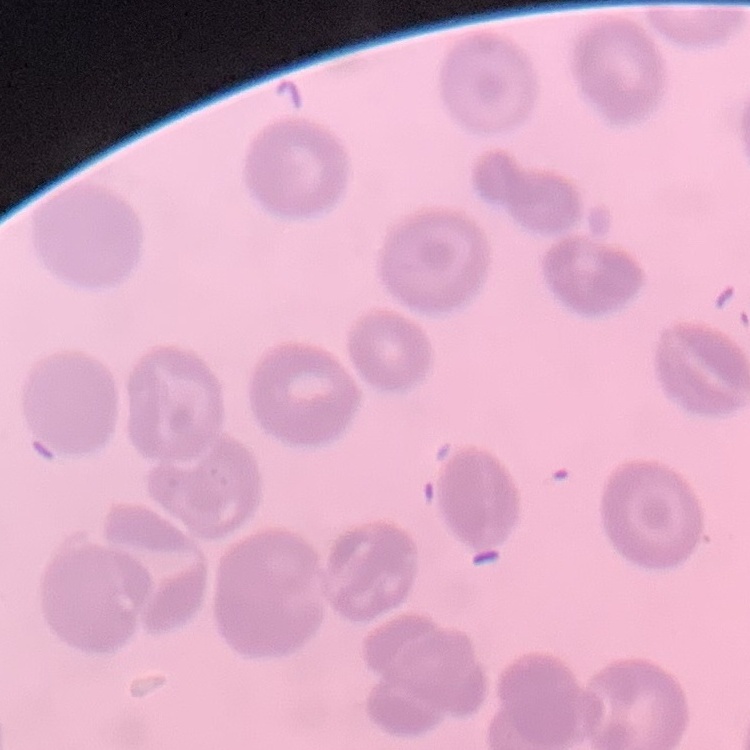

The red blood cells show no rouleaux formation. One tile cut from a larger photomicrograph. Thin blood film. Field's or Giemsa stain.